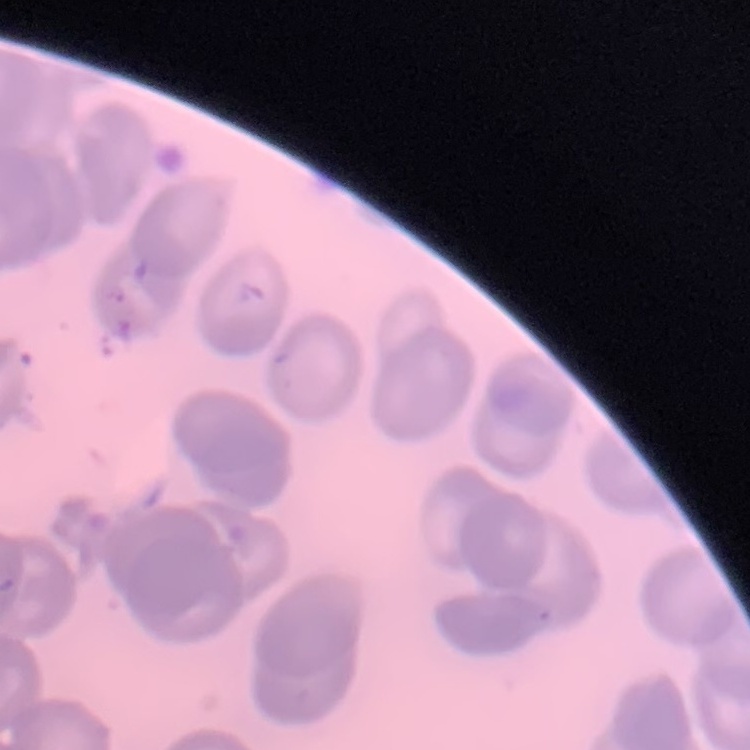
erythrocyte morphology = no rouleaux formation
preparation = thin blood smear
stain = Field's or Giemsa
image type = one tile cut from a larger photomicrograph